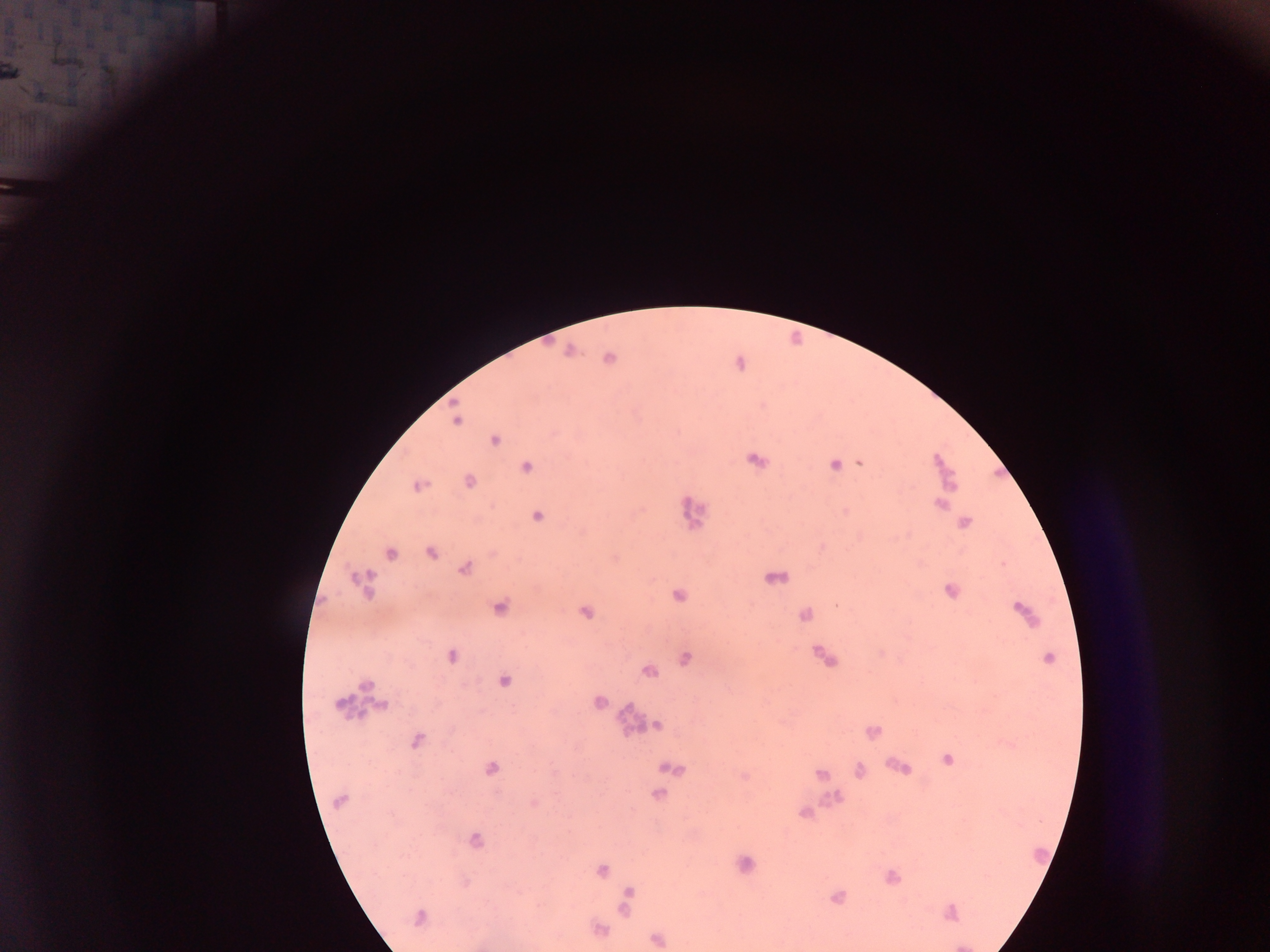
Approximate centers as (x, y) in pixels.
Summary:
  - Leukocyte locations: (945, 469), (357, 696), (627, 721), (832, 800), (1040, 857)
  - Malaria parasite locations: (12, 71), (569, 351), (608, 359), (740, 363), (456, 418), (495, 440), (755, 460), (859, 462), (834, 464), (526, 467), (469, 481), (418, 486), (939, 503), (692, 510), (536, 515), (963, 522), (430, 552), (390, 553), (465, 568), (774, 577), (362, 582), (951, 591), (678, 595), (838, 605), (499, 607), (585, 611), (1023, 613), (805, 614), (451, 655), (823, 657), (684, 658), (1047, 659), (647, 670), (503, 681), (599, 702), (382, 704), (655, 724), (872, 732), (416, 739), (947, 759), (899, 767), (489, 768), (670, 768), (858, 770), (820, 774), (657, 794), (339, 800), (534, 803), (804, 813), (473, 840), (744, 864), (601, 869), (890, 877), (626, 897), (836, 897), (949, 913), (419, 916), (597, 930), (657, 939)
  - Country: Ghana
  - Capture: mobile-phone photograph through a microscope
  - Field of view: single
  - Image size: 1270×952 pixels
  - Preparation: thick blood smear